Identify the preparation type.
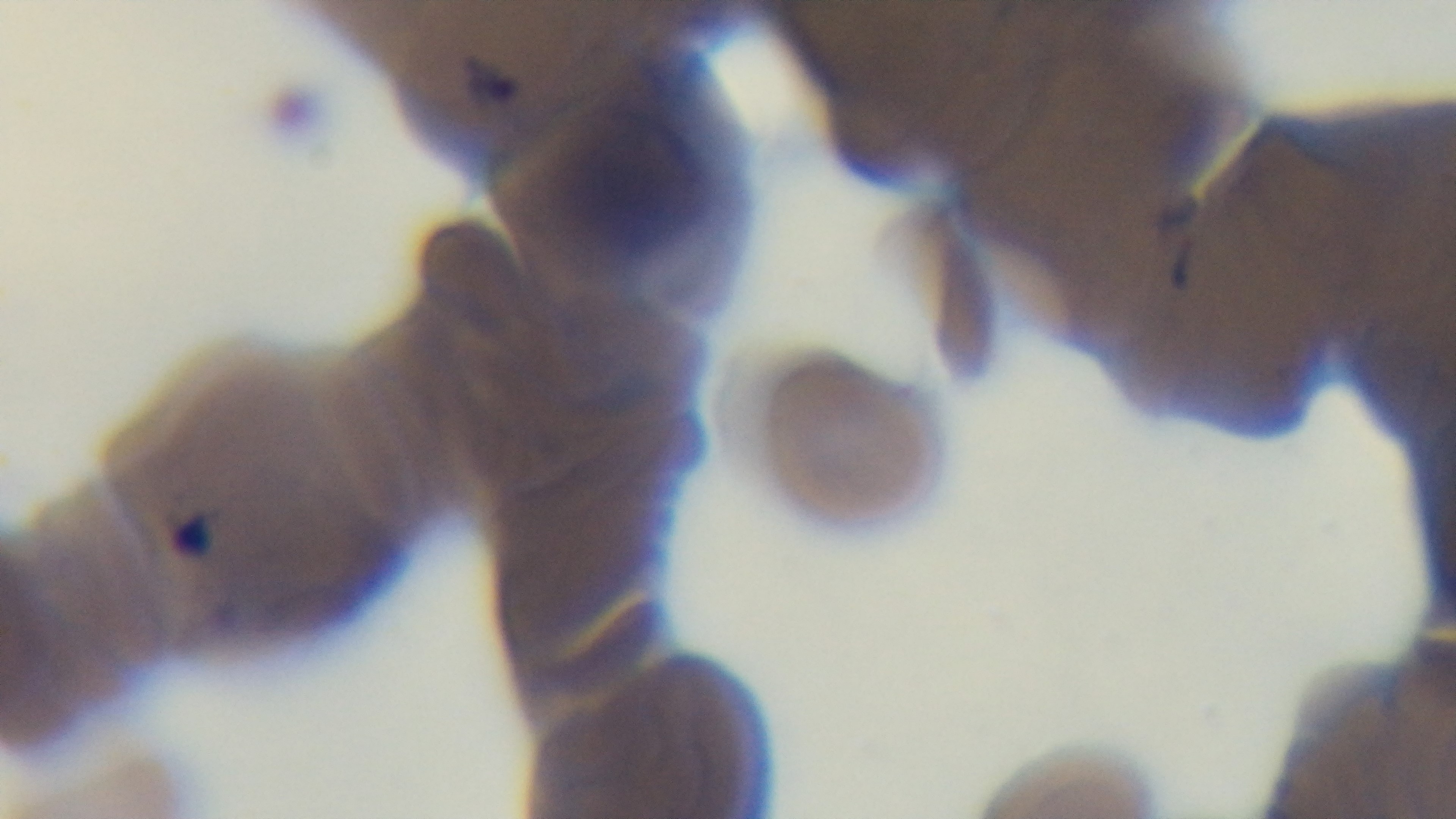
It is a thin blood film.

Summary:
  - Capture: mounted 4K digital camera
  - Stain: Giemsa
  - Objective: 100x oil immersion
  - Field of view: one from the slide
  - Modality: light microscopy
  - Malaria status: positive